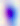
Toxoplasma gondii is shown. 400x magnification. Micrograph.